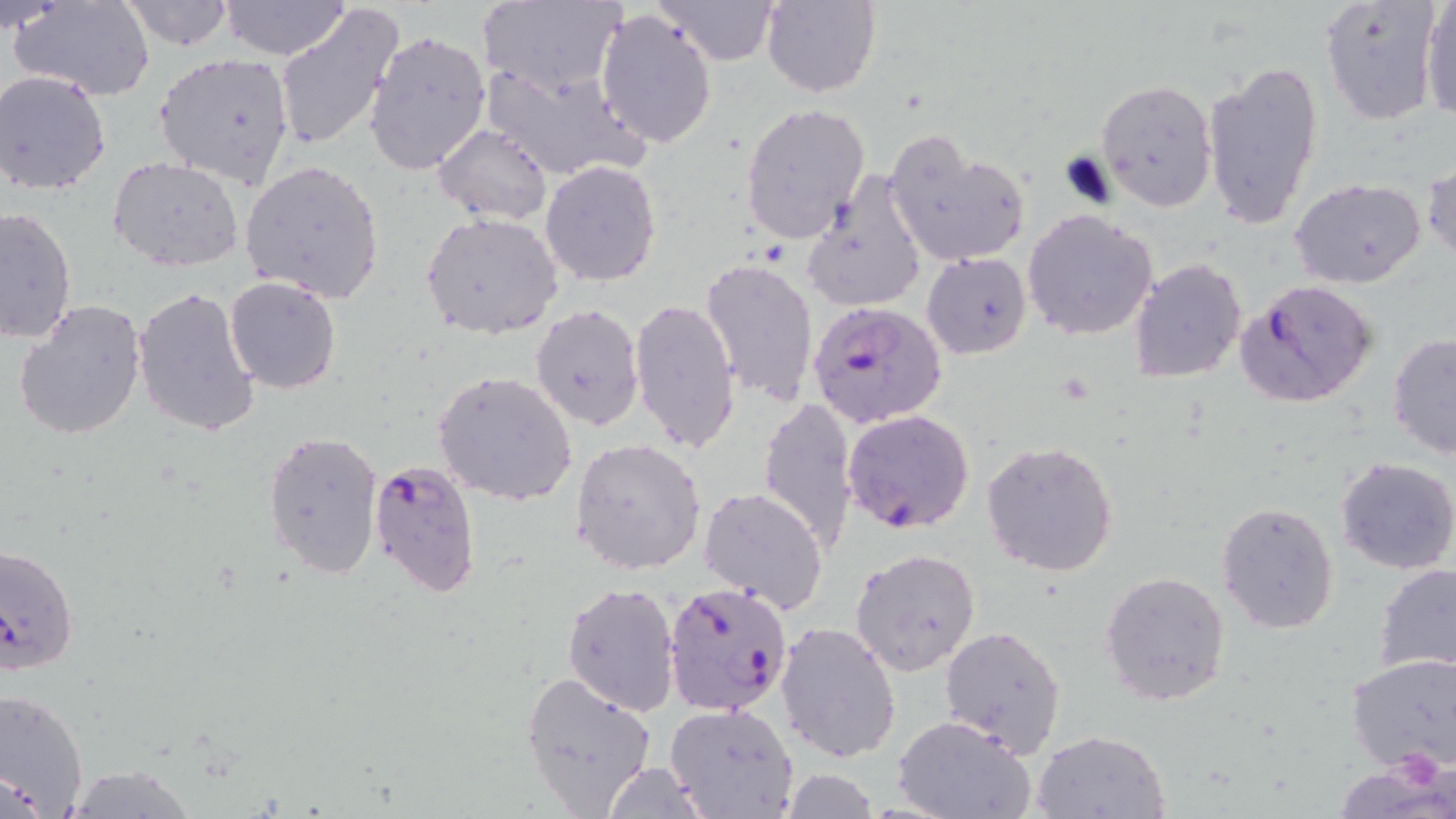

Approximate bounding boxes as [x1, y1, x2, y2] in pixels. Uninfected red blood cell locations: [13, 0, 157, 99], [119, 0, 237, 51], [480, 0, 629, 100], [760, 0, 882, 97], [1421, 0, 1456, 124], [219, 1, 351, 61], [661, 1, 780, 63], [1320, 1, 1442, 128], [274, 2, 403, 153], [1, 3, 69, 35], [595, 8, 718, 151], [363, 30, 490, 177], [154, 53, 298, 189], [1203, 60, 1324, 233], [481, 64, 646, 184], [0, 68, 115, 197], [1096, 77, 1217, 211], [740, 102, 870, 244], [434, 123, 553, 225], [881, 131, 1031, 269], [109, 158, 243, 271], [1422, 158, 1455, 264], [239, 159, 386, 304], [539, 161, 662, 287], [801, 171, 928, 314], [1289, 177, 1427, 289], [0, 204, 77, 344], [1022, 208, 1157, 341], [420, 212, 564, 340], [922, 252, 1032, 358], [699, 256, 819, 405], [1131, 258, 1247, 384], [225, 275, 341, 393], [132, 285, 261, 440], [12, 298, 148, 441], [629, 298, 740, 453], [531, 303, 645, 432], [1387, 335, 1456, 459], [434, 371, 578, 506], [758, 397, 861, 553], [262, 428, 384, 581], [571, 437, 708, 575], [981, 441, 1119, 577], [1334, 456, 1456, 573], [698, 485, 829, 613], [1216, 500, 1340, 634], [850, 547, 981, 677], [1374, 563, 1456, 673], [1100, 569, 1231, 707], [562, 582, 681, 715], [775, 622, 903, 762], [941, 626, 1068, 756], [1346, 652, 1456, 774], [520, 670, 658, 814], [0, 685, 88, 818], [664, 704, 799, 819], [894, 715, 1036, 819], [1031, 729, 1170, 818], [599, 762, 715, 818], [57, 764, 204, 818], [774, 768, 883, 819]. Plasmodium falciparum-infected red blood cell locations: [1235, 279, 1379, 408], [810, 300, 945, 431], [843, 408, 975, 535], [367, 457, 481, 597], [0, 542, 83, 674], [661, 581, 794, 717]. Slide-level diagnosis: Plasmodium falciparum. May-Grünwald-Giemsa stain. Image is 1456×819 pixels. One field of a larger specimen. Light microscopy. Thin blood smear. Captured at 1000x magnification.